Assess for malaria.
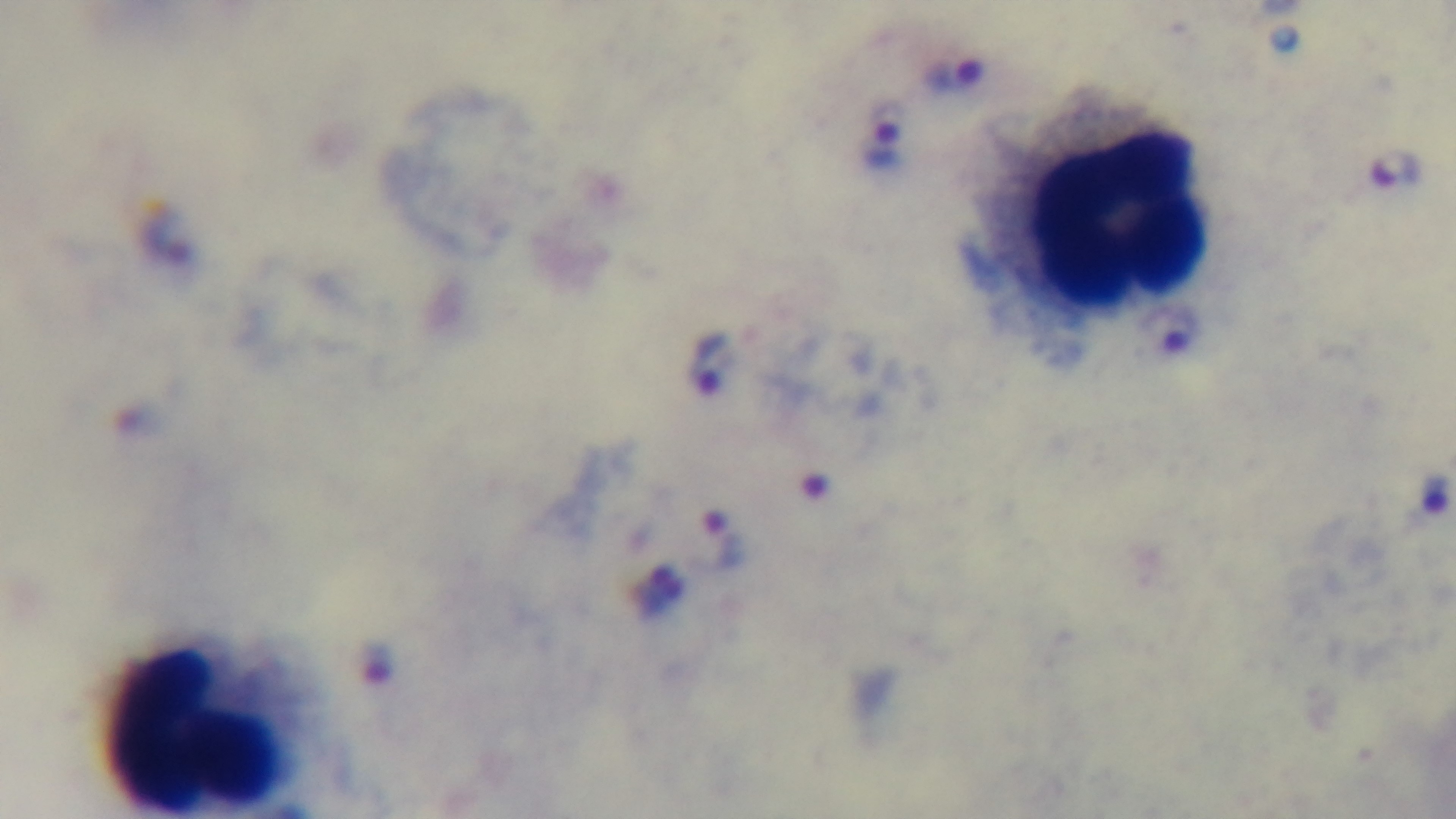
Infected.

modality = light microscopy
stain = Giemsa
capture = mounted 4K digital camera
field of view = one from the slide
preparation = thick
objective = 100x oil immersion